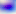

Summary:
  - Identification: Toxoplasma gondii
  - Modality: photomicrograph
  - Magnification: 400x